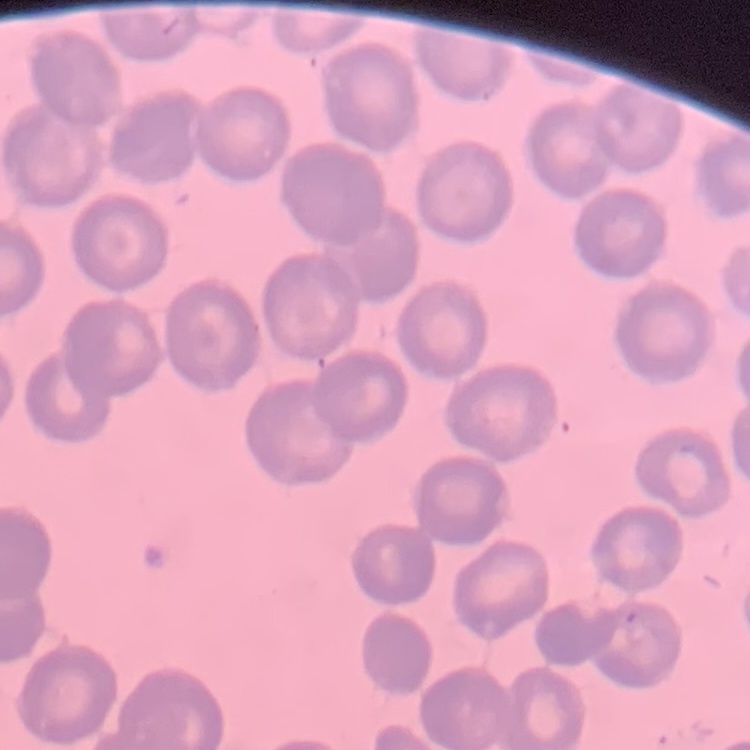
The erythrocytes exhibit no rouleaux formation. Field's or Giemsa stain. One tile cut from a larger photomicrograph. Thin blood smear.